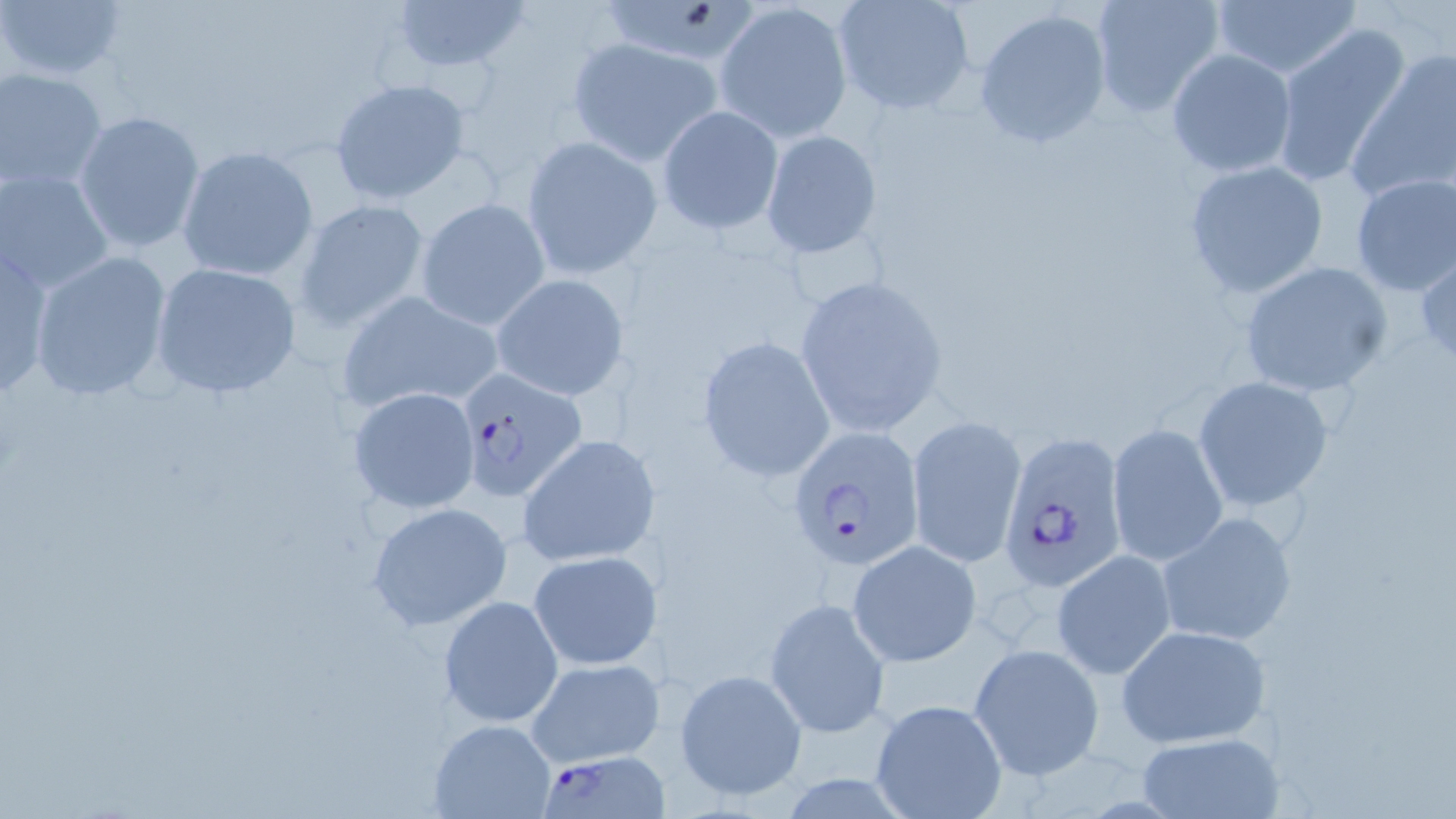

{
  "slide_level_diagnosis": "Plasmodium falciparum",
  "field_of_view": "single",
  "magnification": "1000x",
  "stain": "May-Grünwald-Giemsa",
  "modality": "optical microscopy",
  "plasmodium_falciparum_infected_red_blood_cell_locations": "approximate bounding boxes as (x1, y1, x2, y2) in pixels: (453, 364, 587, 502), (787, 428, 925, 572), (995, 428, 1128, 593), (539, 749, 665, 817)",
  "uninfected_red_blood_cell_locations": "approximate bounding boxes as (x1, y1, x2, y2) in pixels: (1, 0, 128, 84), (389, 0, 532, 77), (602, 0, 768, 63), (831, 0, 977, 116), (1089, 0, 1225, 117), (1211, 1, 1361, 79), (717, 3, 853, 140), (975, 9, 1112, 148), (1271, 23, 1414, 185), (568, 37, 724, 166), (1349, 43, 1456, 200), (1166, 48, 1296, 178), (0, 67, 107, 192), (329, 78, 471, 206), (657, 105, 783, 234), (73, 110, 206, 255), (760, 129, 880, 260), (521, 136, 662, 279), (174, 146, 319, 282), (1184, 160, 1329, 300), (1, 167, 114, 294), (1348, 172, 1456, 299), (415, 198, 550, 329), (293, 199, 432, 332), (0, 243, 59, 396), (27, 251, 173, 402), (1415, 251, 1456, 369), (1240, 259, 1394, 398), (150, 261, 303, 399), (491, 273, 629, 400), (793, 274, 951, 437), (336, 291, 504, 417), (697, 337, 836, 483), (1194, 377, 1334, 510), (348, 385, 480, 513), (906, 414, 1026, 566), (1106, 422, 1228, 567), (517, 433, 660, 568), (367, 502, 513, 632), (1155, 510, 1298, 647), (848, 540, 982, 667), (1052, 549, 1176, 680), (527, 550, 660, 671), (439, 596, 563, 726), (764, 597, 889, 738), (1116, 623, 1271, 749), (968, 642, 1103, 780), (525, 658, 664, 768), (675, 670, 806, 801), (868, 698, 1008, 818), (428, 719, 555, 818), (1135, 734, 1282, 817)",
  "image_size": "1456×819 pixels",
  "preparation": "thin blood film"
}